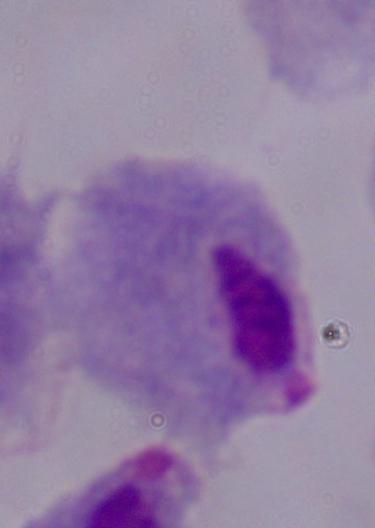
Captured at 1000x magnification. Micrograph. A trichomonad is seen.